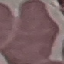
Malaria status: uninfected. Giemsa-stained preparation. Automatically extracted cell patch, resized to 64 × 64 pixels. Thin blood smear. Photographed with a smartphone camera at the microscope eyepiece.